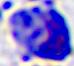 Photomicrograph. 400x magnification. A leukocyte is seen.